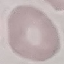

Summary:
  - Malaria status: uninfected
  - Capture: smartphone through the microscope eyepiece
  - Image type: cell patch, automatically extracted from a larger field of view and resized to 64 × 64 pixels
  - Stain: Giemsa
  - Preparation: thin blood smear